Report the malaria status of this cell.
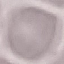
It is uninfected.

Summary:
  - Stain: Giemsa
  - Image type: cell patch, automatically extracted from a larger field of view and resized to 64 × 64 pixels
  - Preparation: thin blood smear
  - Capture: smartphone through the microscope eyepiece